Classify this cell by malaria status.
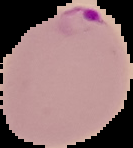
Parasitized.

preparation: thin blood film
image_type: cell region segmented out of the field of view; surrounding area masked to black
image_size: 133×148 pixels